Give the position of every leukocyte visible.
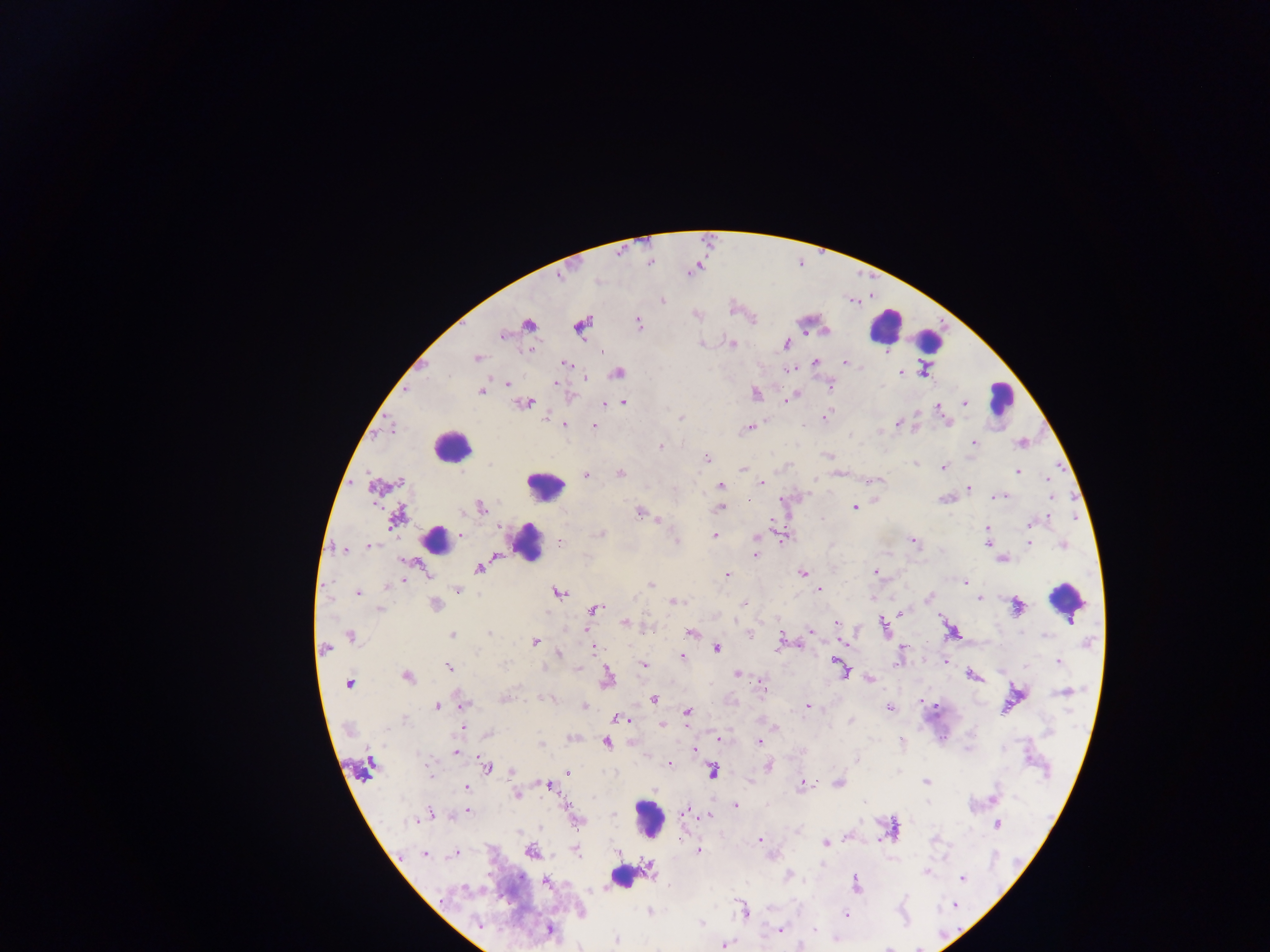
Approximate centers as (x, y) in pixels.
Leukocytes: (885, 326), (930, 340), (1001, 396), (451, 446), (545, 485), (437, 541), (528, 543), (1067, 599), (649, 818), (623, 876).

Malaria parasite locations: (662, 301), (638, 322), (528, 325), (581, 326), (503, 335), (701, 344), (731, 344), (786, 345), (530, 350), (602, 352), (477, 357), (815, 362), (845, 363), (566, 364), (788, 369), (923, 371), (618, 373), (900, 373), (585, 377), (556, 383), (508, 384), (829, 385), (481, 391), (756, 393), (788, 398), (623, 402), (525, 403), (965, 403), (605, 404), (940, 410), (545, 417), (825, 417), (680, 418), (898, 424), (566, 425), (805, 425), (593, 427), (748, 428), (974, 443), (1020, 443), (660, 446), (827, 456), (707, 458), (915, 463), (943, 468), (742, 469), (1018, 471), (621, 474), (586, 476), (1047, 479), (399, 482), (762, 483), (721, 485), (968, 489), (999, 496), (1051, 497), (748, 500), (480, 507), (720, 508), (854, 508), (640, 513), (397, 518), (1048, 518), (1029, 525), (988, 528), (460, 534), (602, 534), (714, 535), (757, 538), (676, 540), (914, 541), (560, 542), (987, 543), (1029, 543), (1063, 544), (369, 546), (344, 550), (756, 555), (1003, 560), (478, 568), (875, 572), (803, 573), (727, 575), (403, 581), (966, 582), (650, 585), (388, 586), (820, 589), (458, 590), (357, 592), (558, 592), (929, 597), (980, 599), (675, 602), (744, 604), (435, 605), (1017, 607), (594, 609), (380, 610), (902, 612), (624, 623), (837, 623), (884, 626), (585, 631), (811, 631), (691, 632), (1022, 633), (489, 634), (750, 634), (452, 635), (1045, 635), (351, 637), (535, 639), (781, 639), (843, 643), (902, 647), (593, 648), (325, 649), (717, 649), (477, 651), (559, 654), (681, 656), (1058, 661), (946, 662), (503, 664), (644, 665), (838, 666), (450, 668), (577, 669), (842, 669), (738, 674), (973, 675), (407, 677), (608, 678), (870, 679), (349, 684), (1065, 691), (503, 699), (551, 699), (653, 699), (463, 705), (437, 706), (584, 706), (807, 707), (889, 707), (935, 707), (687, 712), (619, 719), (404, 720), (851, 721), (663, 725), (464, 728), (776, 728), (489, 734), (718, 738), (759, 741), (902, 742), (607, 743), (541, 744), (694, 750), (456, 752), (856, 760), (370, 763), (669, 764), (768, 766), (487, 767), (430, 771), (512, 771), (713, 771), (568, 772), (925, 782), (838, 784), (548, 785), (804, 785), (467, 788), (517, 795), (995, 798), (736, 807), (686, 810), (467, 811), (431, 813), (709, 816), (413, 821), (578, 821), (997, 824), (797, 830), (760, 840), (825, 843), (698, 850), (531, 851), (576, 851), (618, 852), (425, 855), (455, 855), (649, 869), (925, 872), (789, 875), (963, 879), (547, 882), (855, 884), (465, 888), (955, 905), (744, 910), (649, 911), (845, 914), (700, 922), (479, 924), (549, 930), (779, 930), (814, 930), (616, 939), (724, 946). Thick blood film. One field of view. Sample from Ghana. Mobile-phone photograph taken through the microscope. Image is 1270×952 pixels.